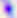

Summary:
  - Magnification: 400x
  - Modality: photomicrograph
  - Identification: Toxoplasma gondii